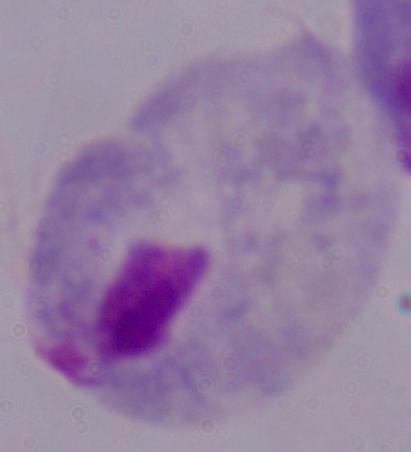

identification: trichomonad
modality: photomicrograph
magnification: 1000x